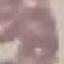 Result: no malaria parasites seen. Cell patch, automatically extracted from a larger field of view and resized to 64 × 64 pixels. Photographed with a smartphone camera at the microscope eyepiece. Giemsa stain. Thin blood film.